Assess this cell for malaria.
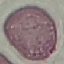
Uninfected.

capture = smartphone through the microscope eyepiece
stain = Giemsa
image type = automatically extracted cell patch, resized to 64 × 64 pixels
preparation = thin smear